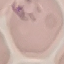
result = no malaria parasites seen
preparation = thin blood film
stain = Giemsa
capture = smartphone camera at the microscope eyepiece
image type = cell patch, automatically extracted from a larger field of view and resized to 64 × 64 pixels